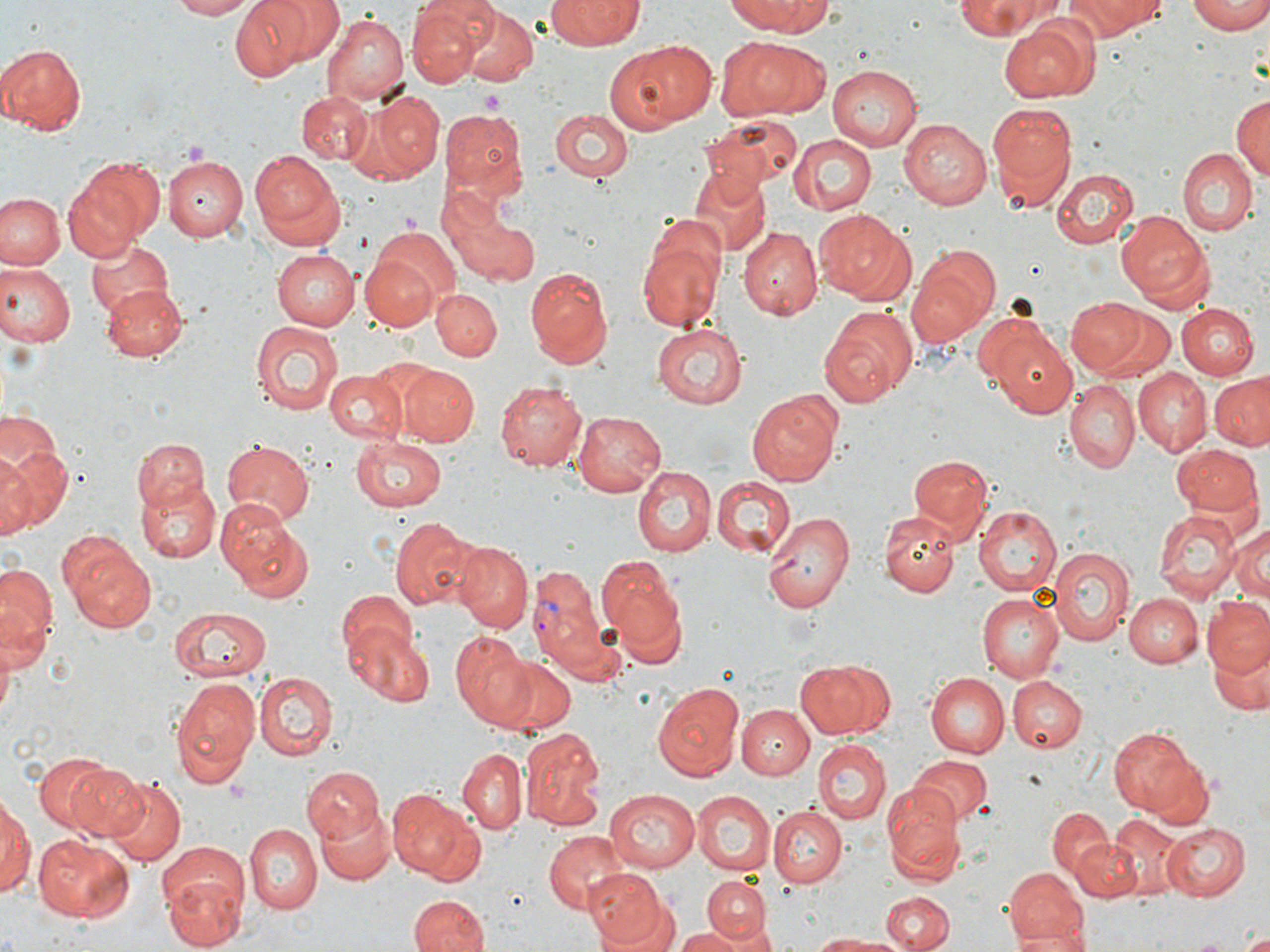
{
  "slide_level_diagnosis": "Plasmodium vivax",
  "platelet_locations": "approximate bounding boxes as [x1, y1, x2, y2] in pixels: [479, 88, 506, 112]",
  "uninfected_red_blood_cell_locations": "approximate bounding boxes as [x1, y1, x2, y2] in pixels: [170, 0, 257, 19], [231, 0, 315, 79], [265, 0, 344, 65], [548, 0, 646, 47], [729, 0, 833, 36], [952, 0, 1064, 38], [1061, 0, 1166, 39], [1187, 0, 1270, 34], [727, 1, 832, 78], [406, 3, 484, 85], [455, 5, 540, 87], [322, 12, 410, 105], [998, 17, 1100, 103], [727, 38, 832, 123], [605, 40, 715, 134], [0, 42, 86, 135], [827, 64, 923, 150], [298, 89, 372, 165], [370, 91, 443, 180], [1230, 94, 1269, 183], [986, 100, 1078, 208], [440, 109, 527, 196], [551, 109, 634, 184], [699, 113, 804, 188], [899, 119, 991, 210], [788, 133, 877, 215], [249, 148, 343, 248], [1178, 148, 1257, 235], [162, 155, 245, 239], [66, 156, 164, 255], [691, 167, 770, 257], [1051, 168, 1138, 249], [0, 192, 63, 271], [436, 194, 528, 338], [453, 209, 538, 287], [1117, 210, 1215, 308], [814, 211, 916, 306], [636, 219, 724, 332], [371, 224, 461, 311], [739, 226, 823, 320], [85, 239, 173, 322], [911, 244, 1001, 337], [274, 247, 360, 330], [362, 255, 438, 329], [0, 261, 74, 348], [524, 266, 614, 367], [105, 284, 186, 359], [430, 289, 500, 361], [1068, 295, 1160, 379], [1176, 304, 1257, 379], [819, 305, 919, 409], [249, 319, 343, 417], [651, 325, 749, 410], [992, 331, 1079, 420], [396, 364, 479, 447], [324, 368, 407, 445], [1135, 369, 1211, 455], [1209, 371, 1270, 451], [494, 379, 588, 473], [1063, 381, 1140, 472], [746, 395, 841, 487], [575, 408, 667, 497], [0, 409, 68, 495], [350, 435, 447, 513], [134, 437, 209, 514], [0, 438, 69, 539], [222, 440, 314, 525], [1170, 445, 1262, 520], [0, 450, 35, 538], [908, 454, 992, 541], [631, 465, 718, 555], [137, 475, 220, 564], [710, 475, 796, 555], [714, 484, 843, 578], [974, 504, 1062, 595], [1154, 507, 1242, 600], [762, 510, 855, 612], [880, 510, 961, 595], [228, 513, 314, 603], [387, 516, 483, 612], [1228, 519, 1269, 604], [57, 532, 156, 634], [452, 540, 532, 632], [1049, 546, 1133, 647], [597, 556, 688, 660], [0, 563, 56, 655], [336, 588, 417, 665], [977, 592, 1065, 681], [1125, 593, 1201, 668], [1203, 598, 1270, 679], [167, 607, 272, 682], [347, 629, 433, 707], [0, 630, 18, 727], [449, 632, 536, 730], [1211, 641, 1267, 715], [488, 654, 579, 737], [793, 659, 895, 738], [253, 672, 334, 758], [926, 673, 1008, 757], [1008, 676, 1087, 753], [167, 677, 260, 788], [651, 680, 746, 784], [738, 703, 813, 779], [1107, 725, 1196, 816], [520, 726, 606, 829], [813, 739, 891, 827], [457, 748, 528, 833], [30, 750, 118, 831], [907, 754, 992, 825], [1149, 756, 1214, 830], [62, 761, 150, 839], [300, 767, 384, 845], [106, 778, 185, 867], [883, 784, 965, 885], [389, 788, 481, 882], [604, 789, 698, 872], [691, 790, 775, 876], [0, 791, 34, 904], [316, 803, 394, 884], [765, 805, 845, 890], [1046, 806, 1114, 880], [1108, 813, 1189, 897], [1164, 822, 1249, 900], [245, 823, 322, 912], [543, 831, 627, 912], [34, 833, 136, 921], [1073, 838, 1140, 900], [156, 843, 247, 923], [1001, 866, 1088, 946], [585, 868, 672, 948], [163, 875, 243, 951], [703, 877, 772, 943], [880, 892, 952, 952], [409, 894, 489, 952], [722, 925, 778, 952], [674, 929, 745, 951], [1007, 929, 1094, 952], [806, 931, 907, 950]",
  "plasmodium_vivax_infected_red_blood_cell_locations": "approximate bounding boxes as [x1, y1, x2, y2] in pixels: [526, 563, 614, 676]",
  "preparation": "thin blood film",
  "field_of_view": "one of a larger specimen",
  "stain": "May-Grünwald-Giemsa",
  "magnification": "1000x",
  "image_size": "1270×952 pixels",
  "modality": "light microscopy"
}